Point out each Plasmodium parasite.
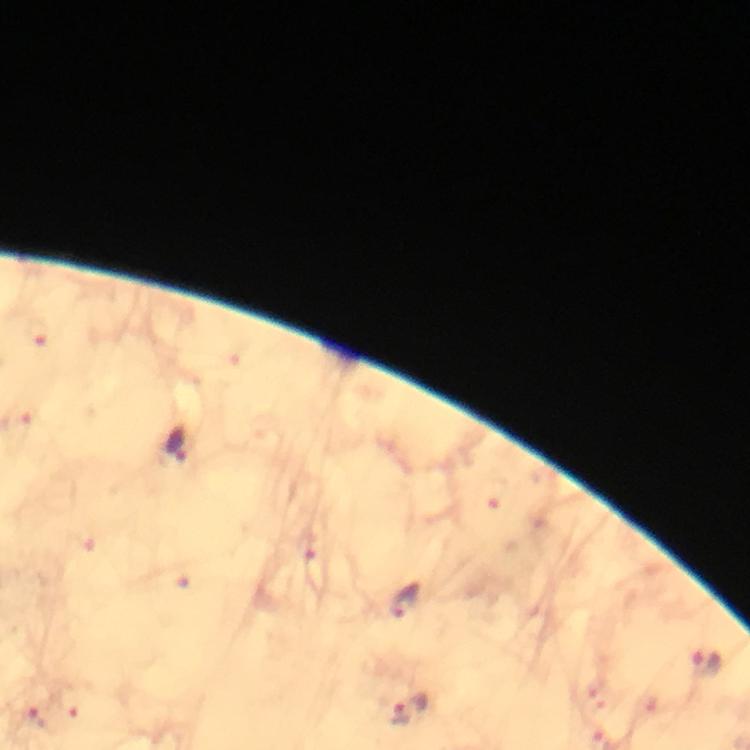
Approximate centers as (x, y) in pixels.
Plasmodium parasites: (38, 332), (177, 444), (309, 547), (406, 601), (707, 665), (409, 709), (37, 718).

At 100x magnification. Smartphone photograph taken through a microscope. Immersion oil applied. Image is 750×750 pixels. Giemsa-stained preparation. Thick blood smear. Cropped region of a single field of view. From a malaria diagnostic workup.